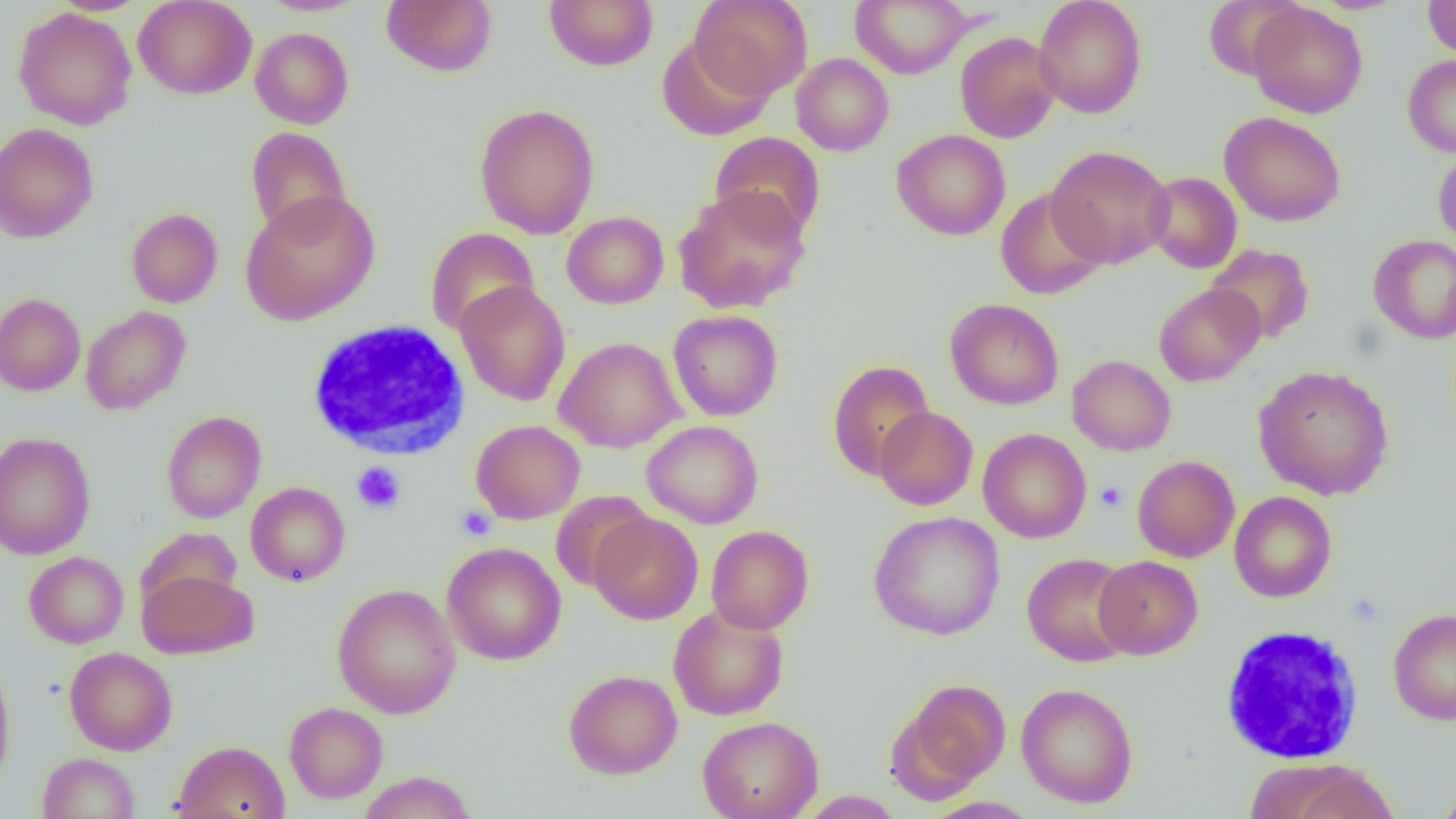

Approximate bounding boxes as [x1, y1, x2, y2] in pixels. Platelet locations: [352, 462, 406, 514], [1095, 482, 1127, 512], [456, 505, 496, 541]. White blood cell locations: [306, 320, 472, 461], [1218, 625, 1365, 764]. Uninfected red blood cell locations: [133, 0, 257, 99], [257, 0, 370, 16], [382, 0, 497, 76], [544, 0, 658, 71], [690, 0, 812, 98], [1034, 0, 1147, 119], [1203, 0, 1303, 81], [1423, 0, 1456, 60], [851, 1, 971, 78], [1247, 2, 1368, 118], [13, 6, 138, 130], [251, 27, 354, 129], [954, 31, 1061, 143], [657, 34, 774, 141], [791, 53, 894, 157], [1402, 55, 1456, 158], [474, 103, 600, 239], [1219, 111, 1346, 226], [0, 123, 99, 243], [245, 127, 351, 238], [891, 129, 1010, 240], [709, 131, 826, 241], [1046, 145, 1174, 268], [1433, 148, 1456, 248], [1143, 171, 1242, 273], [673, 185, 812, 314], [995, 188, 1108, 300], [240, 190, 380, 325], [126, 207, 223, 308], [562, 211, 669, 309], [424, 227, 539, 337], [1368, 234, 1456, 344], [1206, 244, 1315, 344], [455, 280, 571, 406], [1154, 283, 1265, 387], [0, 293, 85, 396], [944, 298, 1064, 410], [80, 306, 191, 415], [668, 310, 783, 421], [554, 337, 685, 453], [1067, 354, 1176, 456], [827, 360, 935, 480], [1253, 365, 1394, 500], [874, 406, 978, 510], [162, 411, 266, 523], [471, 419, 585, 524], [642, 420, 763, 529], [978, 428, 1091, 543], [0, 431, 96, 560], [1132, 455, 1240, 563], [245, 482, 350, 586], [550, 490, 654, 592], [1229, 491, 1337, 602], [868, 510, 1005, 640], [589, 513, 703, 625], [706, 525, 814, 634], [134, 527, 245, 613], [442, 542, 566, 665], [23, 551, 129, 648], [1022, 553, 1137, 666], [1093, 555, 1203, 659], [137, 567, 258, 660], [332, 583, 461, 719], [669, 604, 789, 721], [1388, 607, 1456, 725], [64, 647, 177, 755], [0, 652, 16, 791], [563, 669, 682, 779], [899, 678, 1011, 790], [1016, 683, 1138, 808], [284, 702, 388, 803], [697, 716, 823, 819], [173, 740, 289, 819], [37, 752, 140, 819], [1243, 758, 1387, 818], [357, 771, 478, 818], [1432, 787, 1456, 818], [799, 791, 905, 818]. Slide-level diagnosis: no evidence of blood parasites. Optical microscopy. Single field of view. Captured at 1000x magnification. Image is 1456×819 pixels. Thin blood smear.